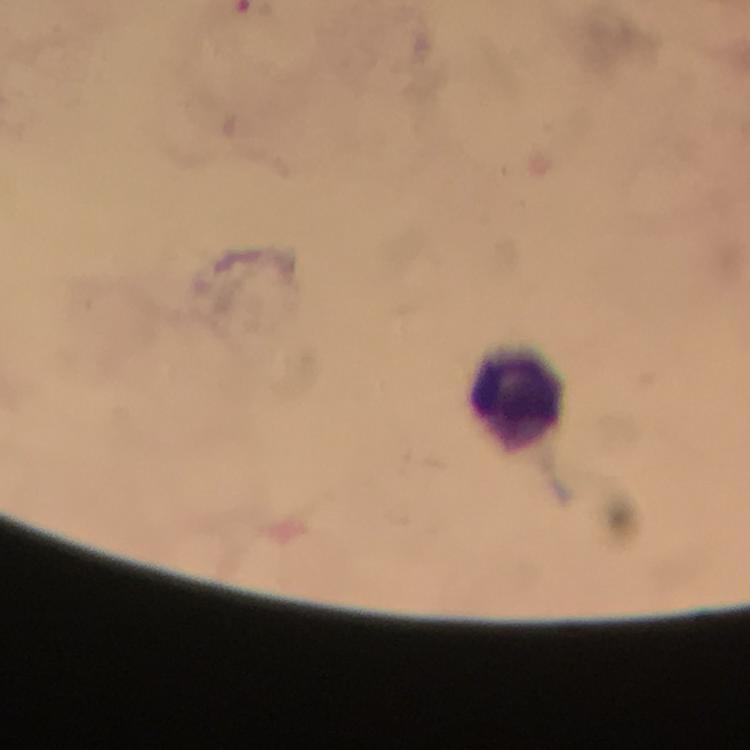

Approximate object centers, in pixels from the top-left corner.
Summary:
  - Leukocyte locations: (x=515, y=393)
  - Immersion oil: used
  - Context: from a malaria diagnostic workup
  - Cropped from: a single field of view
  - Image size: 750×750 pixels
  - Capture: smartphone mounted on the microscope
  - Plasmodium parasites: none detected
  - Stain: Giemsa
  - Preparation: thick blood smear
  - Magnification: 100x